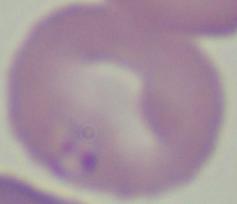

A Babesia parasite is seen. 1000x magnification. Photomicrograph.